State which cell type is depicted.
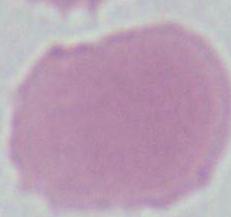

This is an erythrocyte.

Micrograph. Captured at 1000x magnification.